State which parasite is depicted.
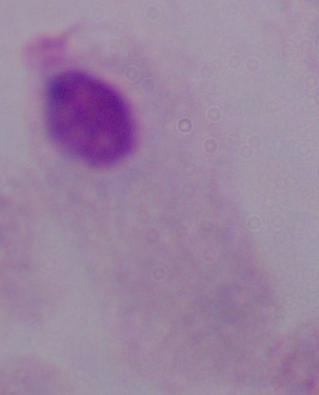
This is a trichomonad.

Summary:
  - Modality: micrograph
  - Magnification: 1000x